Locate every uninfected red blood cell.
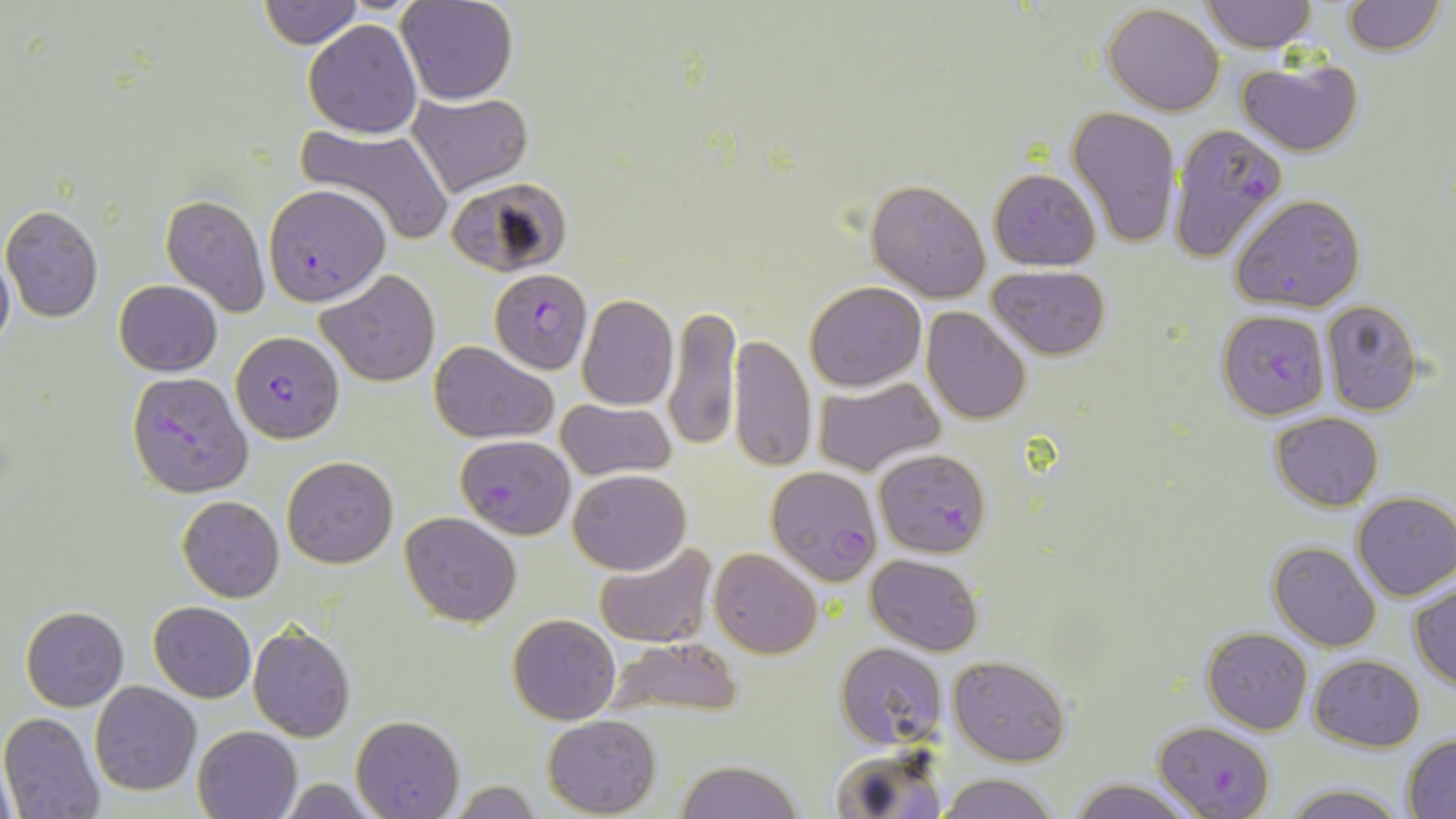

Approximate bounding boxes as [x1, y1, x2, y2] in pixels.
Uninfected red blood cells: [257, 0, 361, 47], [397, 0, 518, 104], [1342, 0, 1445, 54], [1201, 1, 1316, 51], [1102, 4, 1225, 115], [302, 20, 422, 138], [1236, 56, 1364, 157], [406, 90, 531, 197], [1066, 105, 1183, 249], [294, 124, 453, 247], [988, 168, 1101, 271], [865, 177, 992, 302], [446, 178, 572, 276], [159, 191, 270, 318], [1231, 194, 1367, 311], [1, 204, 104, 322], [0, 243, 14, 362], [988, 264, 1110, 360], [319, 269, 437, 386], [113, 280, 223, 377], [805, 281, 926, 390], [577, 294, 678, 409], [1319, 299, 1422, 417], [663, 302, 741, 452], [921, 308, 1032, 425], [730, 333, 817, 472], [431, 341, 557, 444], [811, 375, 946, 477], [555, 399, 677, 482], [1270, 411, 1384, 511], [282, 455, 397, 568], [569, 469, 690, 574], [1352, 493, 1456, 601], [177, 495, 284, 602], [400, 511, 522, 627], [1268, 541, 1381, 651], [594, 543, 717, 649], [710, 548, 821, 658], [865, 554, 982, 656], [1410, 582, 1456, 690], [149, 601, 256, 701], [22, 606, 128, 711], [507, 612, 621, 724], [247, 621, 355, 742], [1202, 627, 1312, 733], [598, 637, 742, 718], [835, 642, 946, 748], [1310, 654, 1425, 750], [948, 655, 1071, 766], [90, 682, 201, 796], [1, 713, 107, 819], [351, 714, 464, 817], [543, 715, 661, 817], [192, 724, 303, 819], [1402, 733, 1456, 816], [829, 743, 947, 819], [676, 760, 804, 818], [937, 772, 1062, 819], [276, 777, 383, 818], [1068, 778, 1199, 818], [451, 780, 544, 817], [1279, 782, 1406, 819].

Summary:
  - Plasmodium falciparum-infected red blood cell locations: [1168, 123, 1289, 262], [263, 184, 390, 304], [489, 269, 593, 382], [1217, 310, 1329, 421], [231, 333, 345, 442], [126, 372, 253, 498], [455, 433, 575, 539], [873, 446, 990, 556], [765, 466, 881, 583], [1156, 720, 1275, 817]
  - Slide-level diagnosis: Plasmodium falciparum
  - Field of view: single
  - Preparation: thin blood film
  - Stain: May-Grünwald-Giemsa
  - Image size: 1456×819 pixels
  - Modality: optical microscopy
  - Magnification: 1000x